Assess the morphology of the erythrocytes.
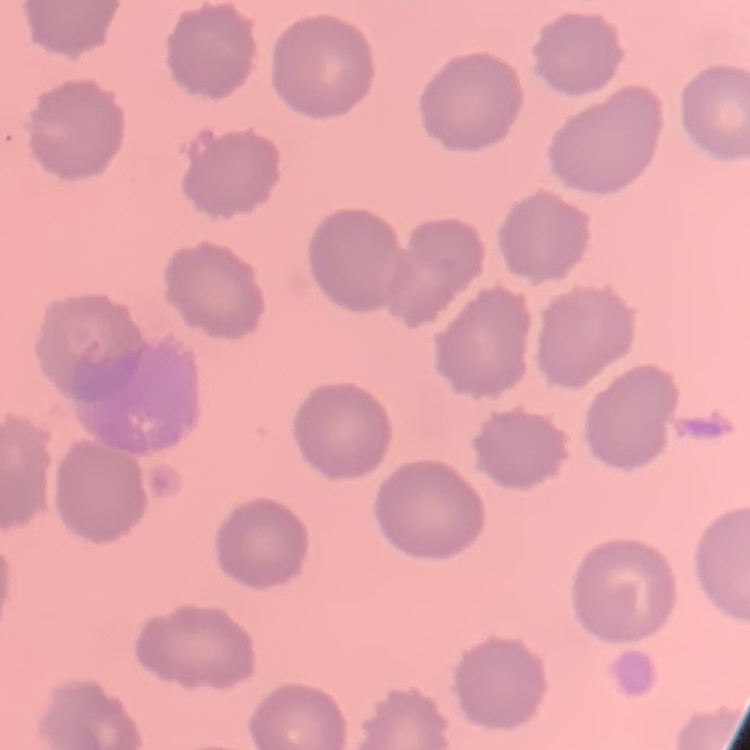

They show no rouleaux formation.

One tile cut from a larger photomicrograph. Stained with either Field's or Giemsa. Thin blood smear.